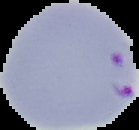 Result: Plasmodium parasites identified. From a thin blood smear. Image is 139×130 pixels. Cell region segmented out of the field of view; the surrounding area is masked to black.